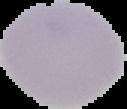

{
  "preparation": "thin blood smear",
  "image_type": "segmented cell region on a black background",
  "image_size": "127×109 pixels",
  "result": "no Plasmodium parasites seen"
}